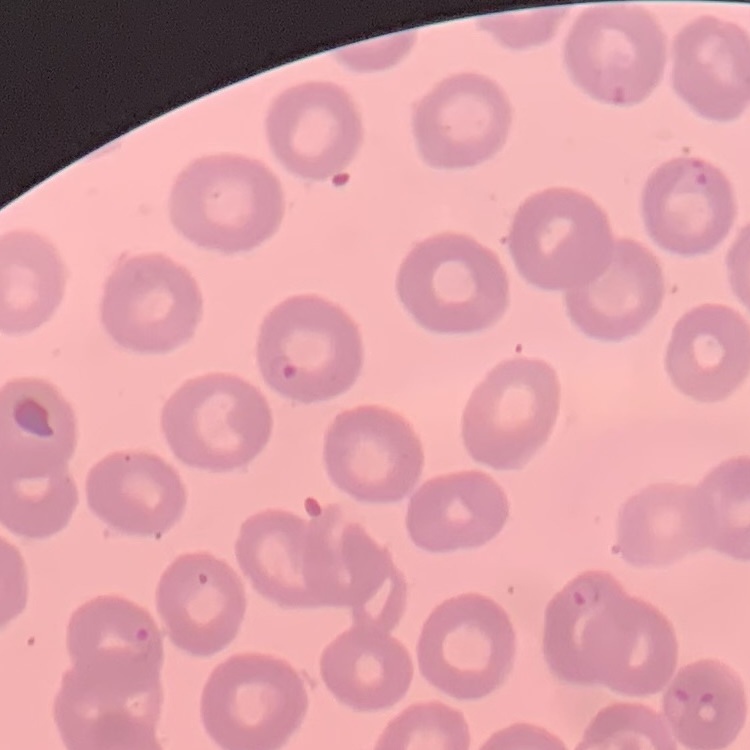

erythrocyte morphology = no rouleaux formation
preparation = thin peripheral smear
image type = one tile cut from a larger photomicrograph
stain = Field's or Giemsa